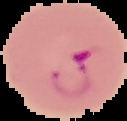
Summary:
  - Preparation: thin blood smear
  - Image type: segmented cell region on a black background
  - Image size: 127×121 pixels
  - Result: Plasmodium parasites detected